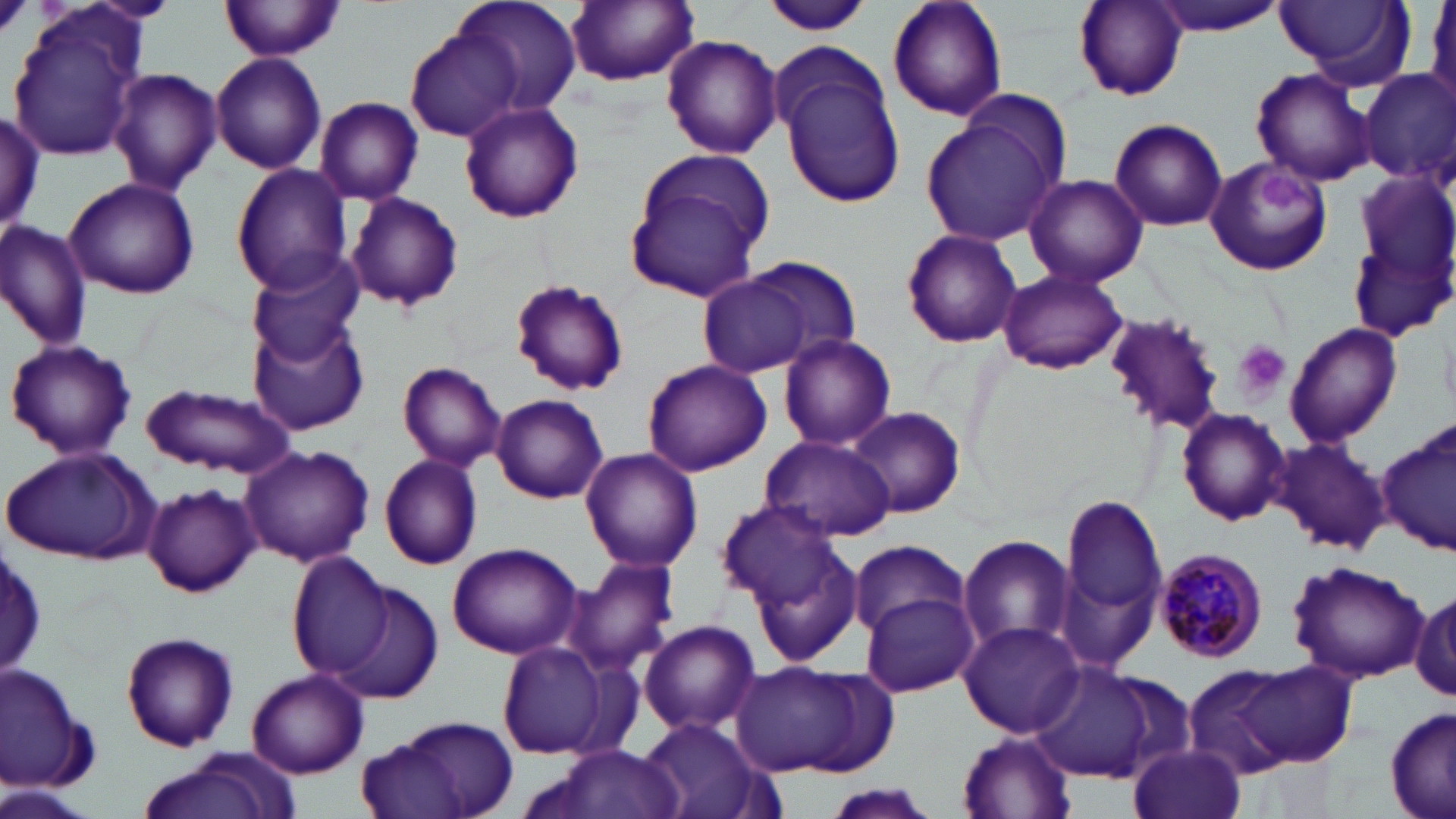 Approximate bounding boxes as (x1,y1)-(x2,y2) corner pairs in pixels. Plasmodium malariae-infected red blood cell locations: (1154,546)-(1269,662). Uninfected red blood cell locations: (221,0)-(344,62), (449,0)-(583,117), (759,0)-(872,36), (885,0)-(1009,123), (1070,0)-(1188,104), (1146,0)-(1287,37), (1274,0)-(1412,88), (564,2)-(700,87), (8,7)-(149,165), (405,28)-(522,144), (661,32)-(782,159), (770,42)-(907,212), (210,52)-(327,175), (1250,66)-(1380,186), (108,68)-(224,195), (1358,69)-(1456,186), (314,95)-(423,205), (457,100)-(585,223), (0,109)-(46,234), (920,112)-(1063,247), (1109,118)-(1227,232), (622,147)-(777,301), (1203,156)-(1334,277), (231,163)-(353,294), (1356,170)-(1455,280), (1023,173)-(1148,288), (64,176)-(199,300), (343,193)-(464,312), (0,219)-(94,349), (901,229)-(1024,349), (1349,243)-(1448,338), (244,250)-(367,365), (722,254)-(862,368), (998,269)-(1130,375), (510,280)-(628,397), (1104,310)-(1229,431), (249,319)-(368,437), (1285,322)-(1400,446), (777,333)-(897,451), (5,338)-(138,461), (642,359)-(772,475), (396,361)-(508,471), (144,383)-(297,478), (491,393)-(608,504), (846,406)-(965,519), (1176,407)-(1290,526), (1380,422)-(1456,558), (759,434)-(896,542), (1271,437)-(1391,555), (240,445)-(374,570), (2,447)-(158,564), (579,448)-(702,574), (378,454)-(483,570), (141,484)-(260,598), (1063,494)-(1167,627), (715,501)-(847,612), (732,529)-(867,669), (956,534)-(1076,654), (847,540)-(970,637), (446,542)-(583,660), (1,544)-(46,680), (284,553)-(401,682), (569,557)-(681,676), (1287,559)-(1427,682), (329,581)-(444,702), (861,591)-(980,696), (1412,591)-(1456,701), (639,620)-(760,735), (958,621)-(1085,738), (120,630)-(240,752), (497,641)-(616,761), (734,659)-(894,779), (1239,660)-(1359,766), (1030,662)-(1173,784), (1,664)-(93,794), (1183,664)-(1297,777), (1091,668)-(1202,781), (248,669)-(368,778), (1385,707)-(1455,819), (363,716)-(522,819), (640,718)-(773,819), (957,730)-(1081,817), (525,743)-(691,818), (1131,744)-(1245,819), (135,752)-(296,819), (2,783)-(92,819), (820,786)-(944,819). Platelet locations: (1253,170)-(1320,217), (1235,341)-(1289,398). Slide-level diagnosis: Plasmodium malariae. One field of a larger specimen. 1000x magnification. May-Grünwald-Giemsa-stained preparation. Thin blood smear. Image is 1456×819 pixels. Optical microscopy.